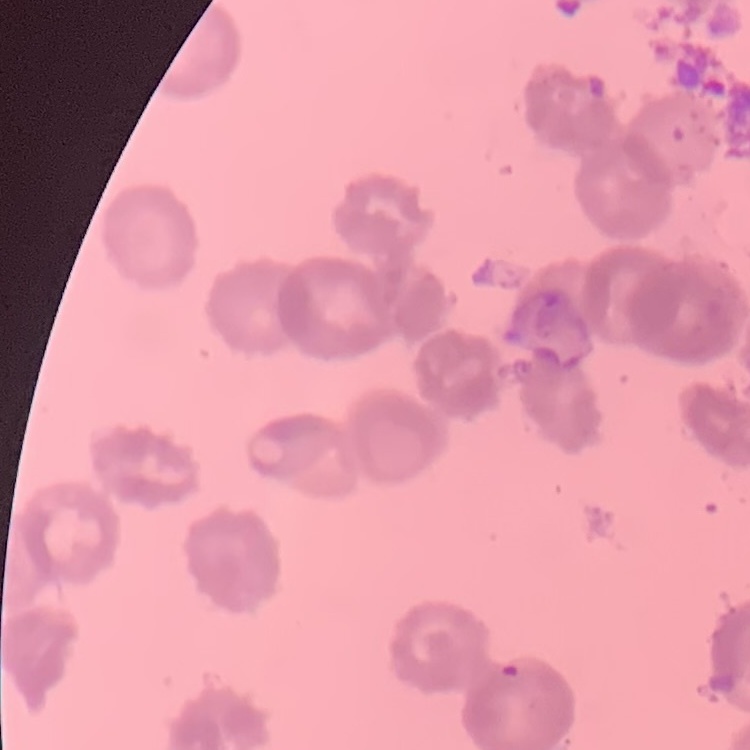

Summary:
  - Red blood cell morphology: rouleaux formation
  - Preparation: thin blood film
  - Stain: Field's or Giemsa
  - Image type: one tile cut from a larger photomicrograph